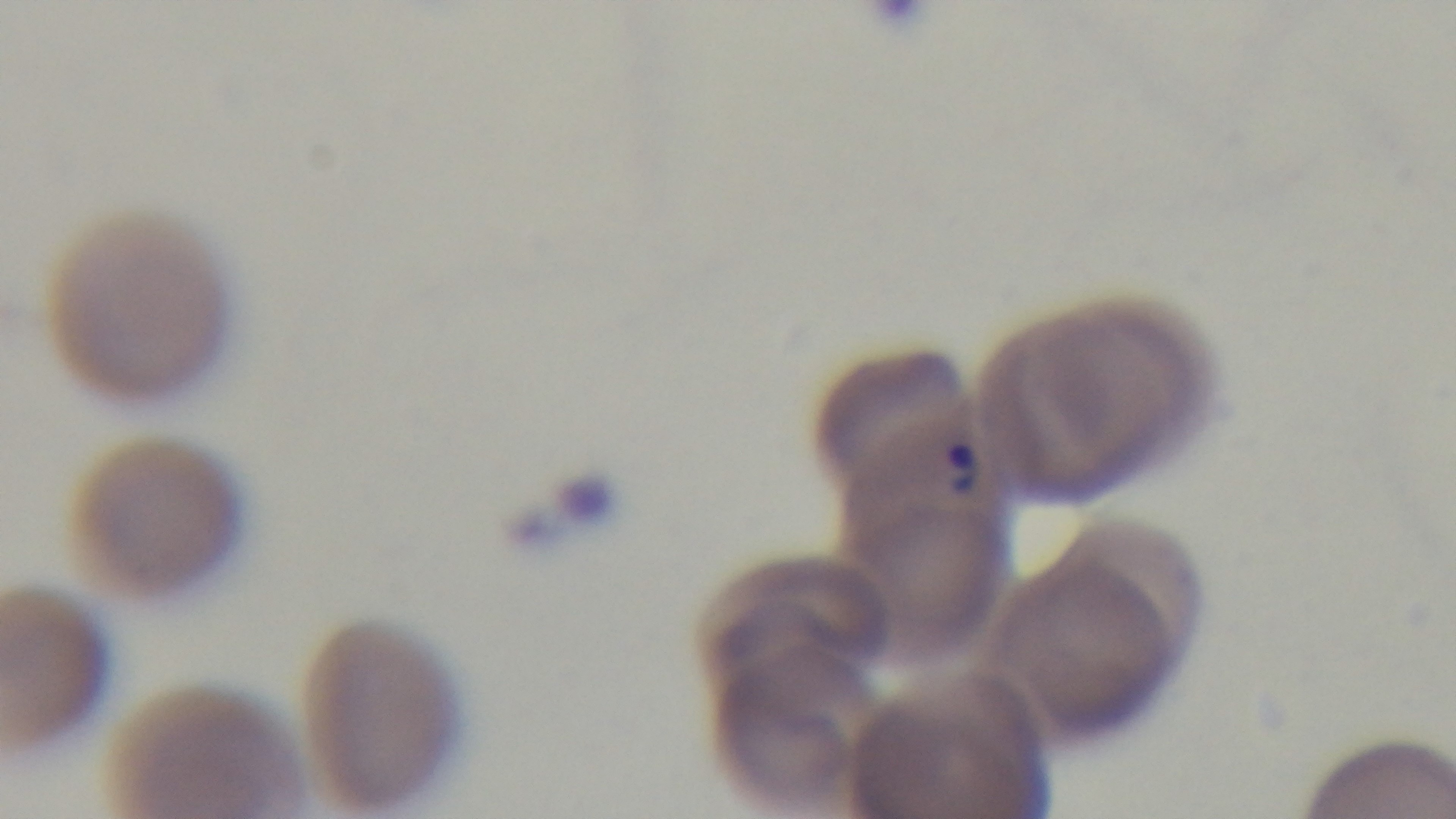
Mounted 4K digital camera. Giemsa stain. Preparation: thin blood film. Malaria status: infected. Single field of view. Photomicrograph. Oil-immersion objective, 100x.